Identify the parasite.
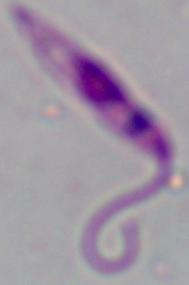
This is Leishmania.

Summary:
  - Modality: photomicrograph
  - Magnification: 1000x